Locate and identify every blood parasite.
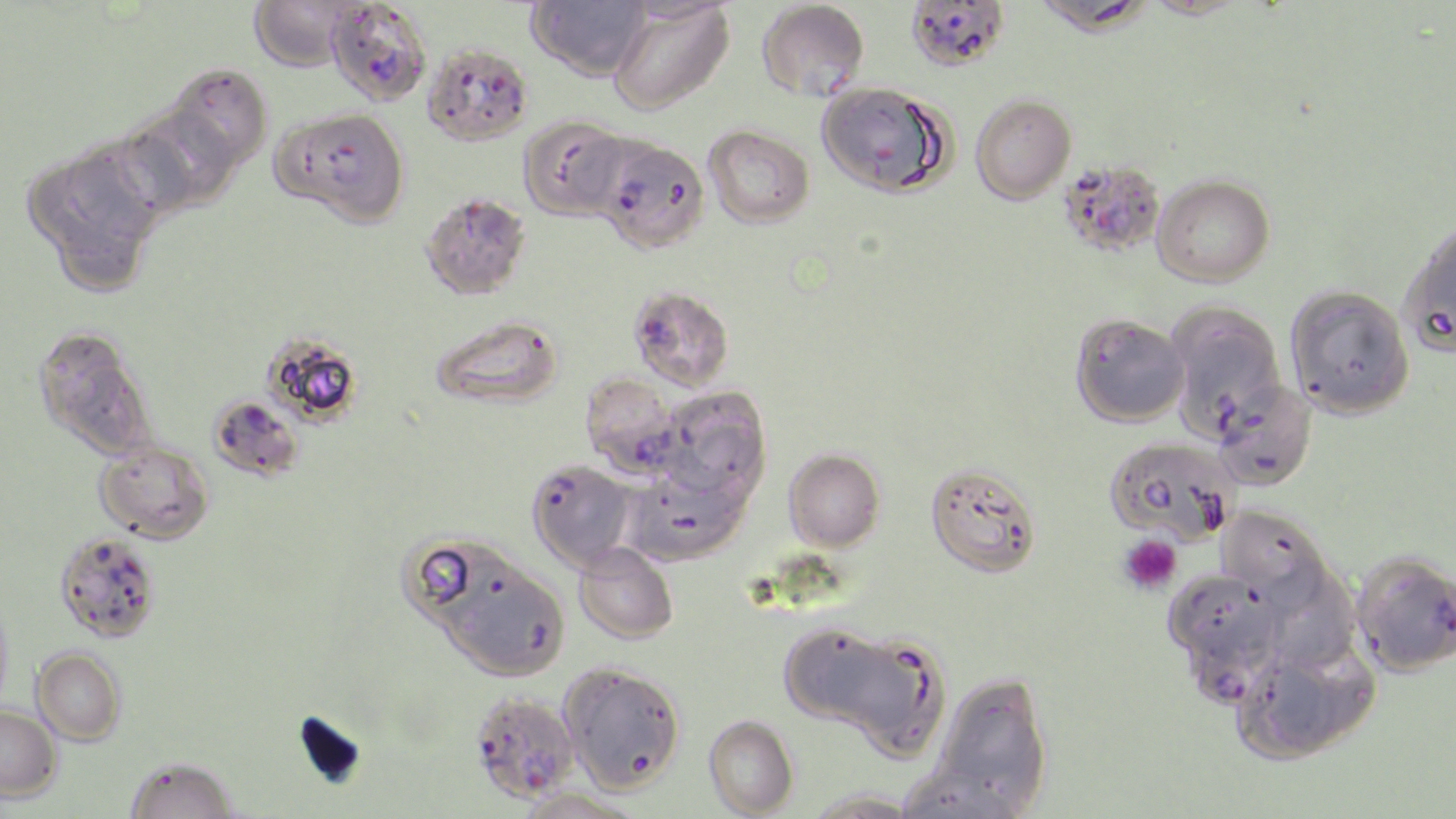

Approximate bounding boxes as (x1,y1)-(x2,y2) corner pairs in pixels.
Plasmodium falciparum-infected red blood cells: (328,2)-(431,109), (422,44)-(533,147), (593,136)-(710,253), (1058,160)-(1166,258), (628,285)-(735,391), (580,372)-(686,478), (207,394)-(304,482), (526,459)-(637,571), (1351,550)-(1456,677), (1171,620)-(1284,704), (468,690)-(579,804).
No Plasmodium ovale, Plasmodium malariae, Plasmodium vivax, Babesia divergens, or Trypanosoma brucei observed.

Platelet locations: (1118,534)-(1182,595). Uninfected red blood cell locations: (248,0)-(359,72), (527,0)-(651,80), (906,0)-(1010,71), (757,1)-(869,101), (1031,1)-(1154,36), (607,2)-(734,116), (166,66)-(272,173), (816,82)-(952,197), (970,93)-(1076,204), (273,106)-(410,227), (124,107)-(237,214), (518,115)-(632,221), (704,125)-(815,228), (25,145)-(163,288), (1152,175)-(1275,287), (420,191)-(532,300), (1398,219)-(1456,358), (1284,284)-(1415,420), (1164,301)-(1287,440), (430,314)-(565,409), (1070,314)-(1189,427), (32,325)-(157,459), (262,331)-(364,426), (1212,380)-(1317,491), (657,387)-(772,503), (1104,436)-(1238,547), (94,440)-(214,544), (783,448)-(886,552), (924,461)-(1043,579), (623,464)-(751,567), (1217,504)-(1332,610), (53,532)-(162,643), (401,536)-(517,634), (574,543)-(679,644), (439,558)-(570,681), (1267,564)-(1360,673), (0,593)-(15,716), (779,623)-(896,728), (852,638)-(951,769), (1240,644)-(1379,763), (32,647)-(127,745), (558,661)-(687,795), (930,673)-(1054,814), (0,704)-(61,802), (703,714)-(799,818), (124,756)-(239,818), (895,768)-(1024,819), (513,788)-(646,819), (802,789)-(926,818). Slide-level diagnosis: Plasmodium falciparum. Thin blood smear. One field of a larger specimen. Optical microscopy. Image is 1456×819 pixels. Captured at 1000x magnification. May-Grünwald-Giemsa-stained preparation.